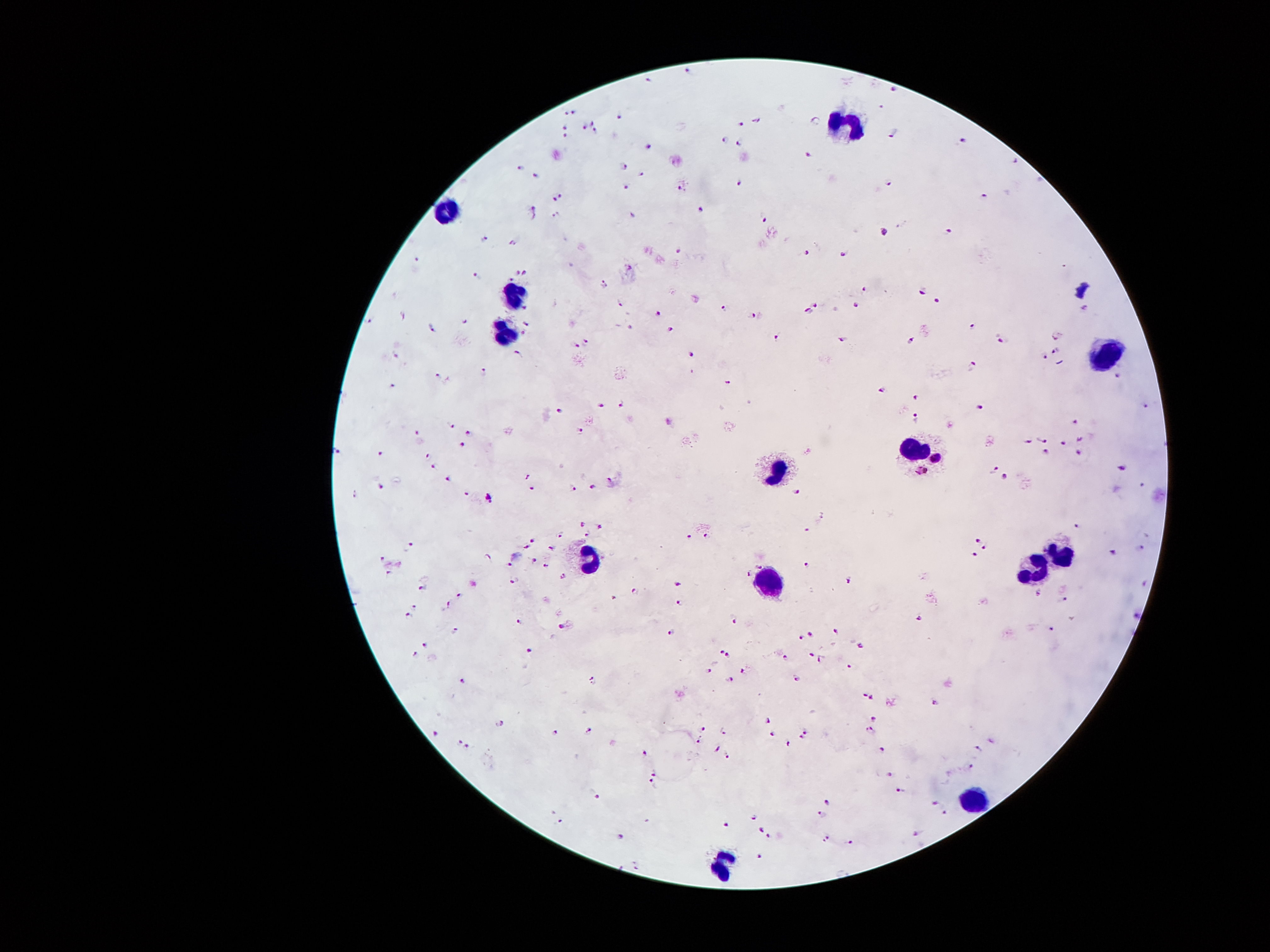
coordinate format = approximate centers as (x, y) in pixels
Plasmodium parasite locations = (690, 69), (645, 81), (894, 91), (881, 105), (574, 112), (564, 114), (619, 114), (757, 119), (591, 120), (816, 120), (741, 122), (564, 127), (584, 127), (596, 132), (895, 132), (566, 135), (722, 140), (965, 140), (739, 143), (647, 145), (810, 153), (1017, 158), (625, 165), (522, 168), (642, 171), (536, 173), (741, 179), (887, 183), (627, 186), (683, 186), (561, 196), (983, 198), (553, 201), (701, 209), (533, 212), (554, 214), (632, 216), (764, 219), (950, 230), (886, 232), (484, 239), (513, 242), (680, 247), (806, 254), (844, 254), (416, 258), (515, 270), (526, 275), (475, 277), (510, 278), (602, 283), (864, 285), (923, 291), (937, 300), (619, 301), (525, 306), (815, 306), (858, 306), (726, 308), (808, 309), (1083, 309), (658, 313), (757, 316), (401, 318), (466, 319), (368, 323), (527, 323), (973, 324), (632, 326), (431, 328), (670, 331), (523, 334), (1055, 336), (778, 337), (843, 339), (912, 339), (1001, 339), (586, 341), (576, 346), (1054, 349), (517, 352), (396, 354), (691, 354), (1044, 357), (974, 365), (484, 372), (1116, 374), (438, 375), (727, 380), (391, 385), (882, 390), (917, 397), (622, 405), (601, 407), (1146, 407), (979, 408), (559, 412), (917, 415), (1072, 420), (452, 423), (414, 430), (579, 430), (469, 431), (1078, 438), (1040, 440), (1026, 441), (1062, 441), (461, 444), (1047, 449), (337, 451), (378, 451), (1080, 453), (428, 456), (433, 468), (994, 468), (1123, 469), (527, 476), (1006, 476), (449, 479), (610, 479), (1142, 481), (594, 484), (380, 486), (576, 486), (531, 487), (797, 491), (466, 492), (358, 494), (489, 500), (821, 519), (584, 522), (1080, 523), (601, 525), (805, 530), (587, 532), (559, 535), (688, 535), (706, 535), (533, 537), (978, 540), (410, 545), (527, 547), (550, 547), (983, 548), (1139, 548), (1113, 551), (973, 553), (380, 558), (487, 560), (512, 565), (543, 565), (806, 565), (759, 568), (749, 571), (386, 576), (564, 576), (515, 579), (678, 581), (848, 583), (1146, 583), (423, 586), (637, 591), (1037, 593), (461, 594), (612, 599), (1067, 599), (675, 604), (411, 606), (446, 607), (410, 614), (515, 617), (918, 617), (734, 622), (563, 624), (456, 627), (1050, 627), (834, 630), (666, 634), (810, 634), (802, 635), (426, 642), (862, 645), (719, 649), (413, 654), (530, 654), (729, 655), (810, 655), (783, 657), (821, 660), (849, 667), (708, 670), (741, 670), (796, 677), (462, 678), (731, 678), (591, 679), (865, 692), (871, 697), (935, 701), (769, 718), (876, 718), (500, 723), (703, 728), (591, 729), (806, 730), (870, 730), (554, 732), (724, 732), (434, 733), (772, 735), (802, 737), (458, 741), (696, 741), (787, 744), (468, 746), (882, 746), (719, 747), (978, 748), (645, 755), (727, 756), (972, 765), (655, 775), (888, 775), (651, 783), (897, 788), (597, 794), (826, 802), (937, 802), (944, 812), (820, 813), (754, 816), (560, 823), (726, 823), (760, 827), (914, 835), (620, 837), (768, 837), (825, 837), (851, 842), (757, 856), (637, 868)
leukocyte locations = (846, 123), (445, 207), (514, 295), (503, 326), (1102, 348), (915, 444), (774, 471), (1060, 547), (590, 558), (1033, 566), (766, 581), (972, 795), (713, 864)
stain = Giemsa
capture = smartphone camera through the microscope eyepiece
magnification = 100x
preparation = thick peripheral-blood smear
image size = 1270×952 pixels
field of view = single
patient malaria status = positive for Plasmodium falciparum